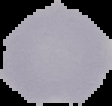

Summary:
  - Image type: segmented cell region with the area outside set to black
  - Result: no malaria parasites seen
  - Preparation: thin blood smear
  - Image size: 112×106 pixels